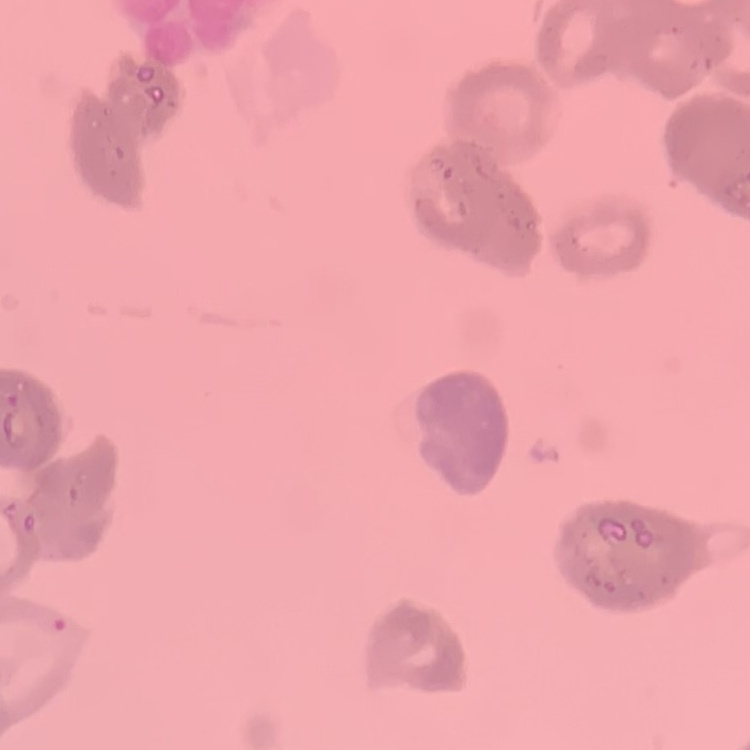 The erythrocytes exhibit rouleaux formation. Stained with either Field's or Giemsa. Thin blood film. One tile cut from a larger photomicrograph.